Name the parasite shown.
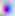

This is Toxoplasma gondii.

Summary:
  - Magnification: 400x
  - Modality: photomicrograph